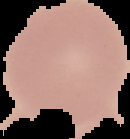

Summary:
  - Malaria status: uninfected
  - Preparation: thin blood film
  - Image size: 130×139 pixels
  - Image type: segmented cell region with the area outside set to black